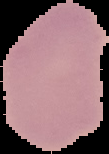
Summary:
  - Result: negative for malaria parasites
  - Image type: segmented cell region on a black background
  - Image size: 109×154 pixels
  - Preparation: thin blood film